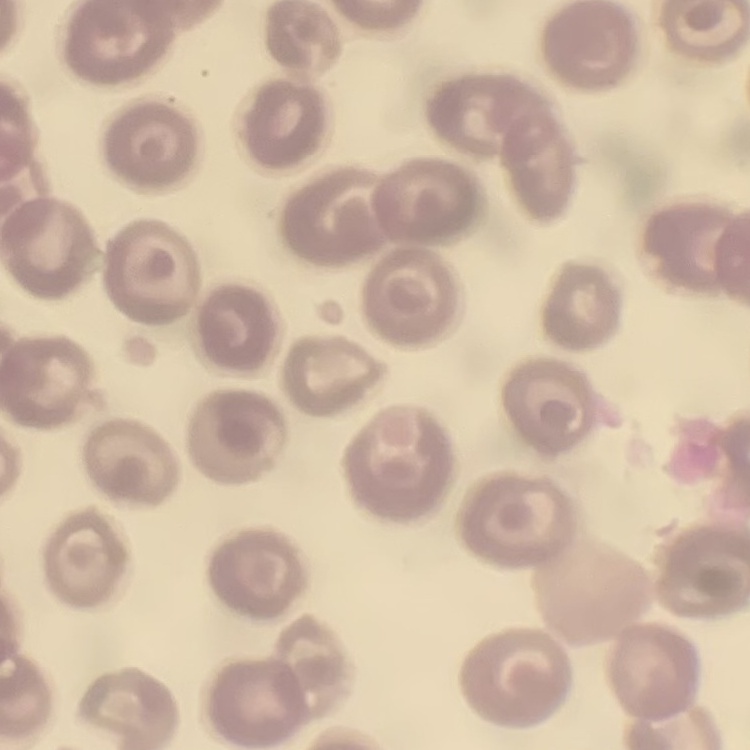
The erythrocytes exhibit no rouleaux formation. One tile cut from a larger photomicrograph. Thin peripheral smear. Stained with either Field's or Giemsa.